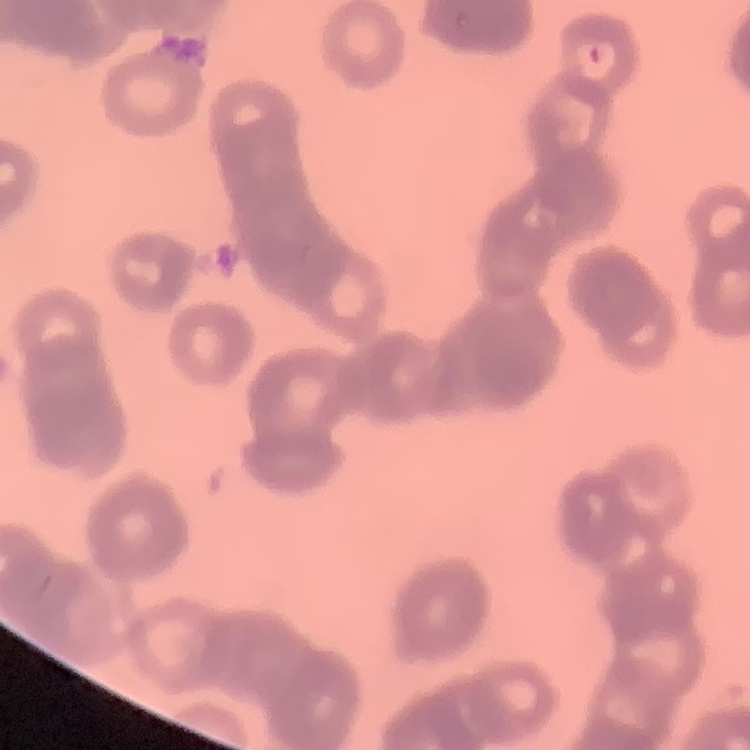
Summary:
  - Red blood cell morphology: rouleaux formation
  - Stain: Field's or Giemsa
  - Preparation: thin peripheral smear
  - Image type: square crop of a larger photomicrograph